Assess this cell for malaria.
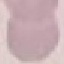

Uninfected.

Automatically extracted cell patch, resized to 64 × 64 pixels. Giemsa stain. Photographed with a smartphone camera at the microscope eyepiece. Thin blood smear.